Name the parasite shown.
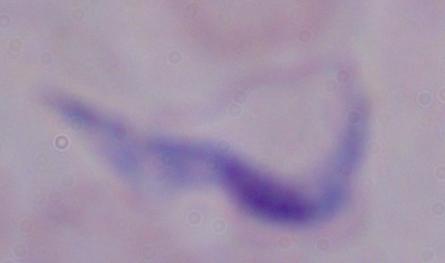
This is a trypanosome.

Summary:
  - Modality: photomicrograph
  - Magnification: 1000x